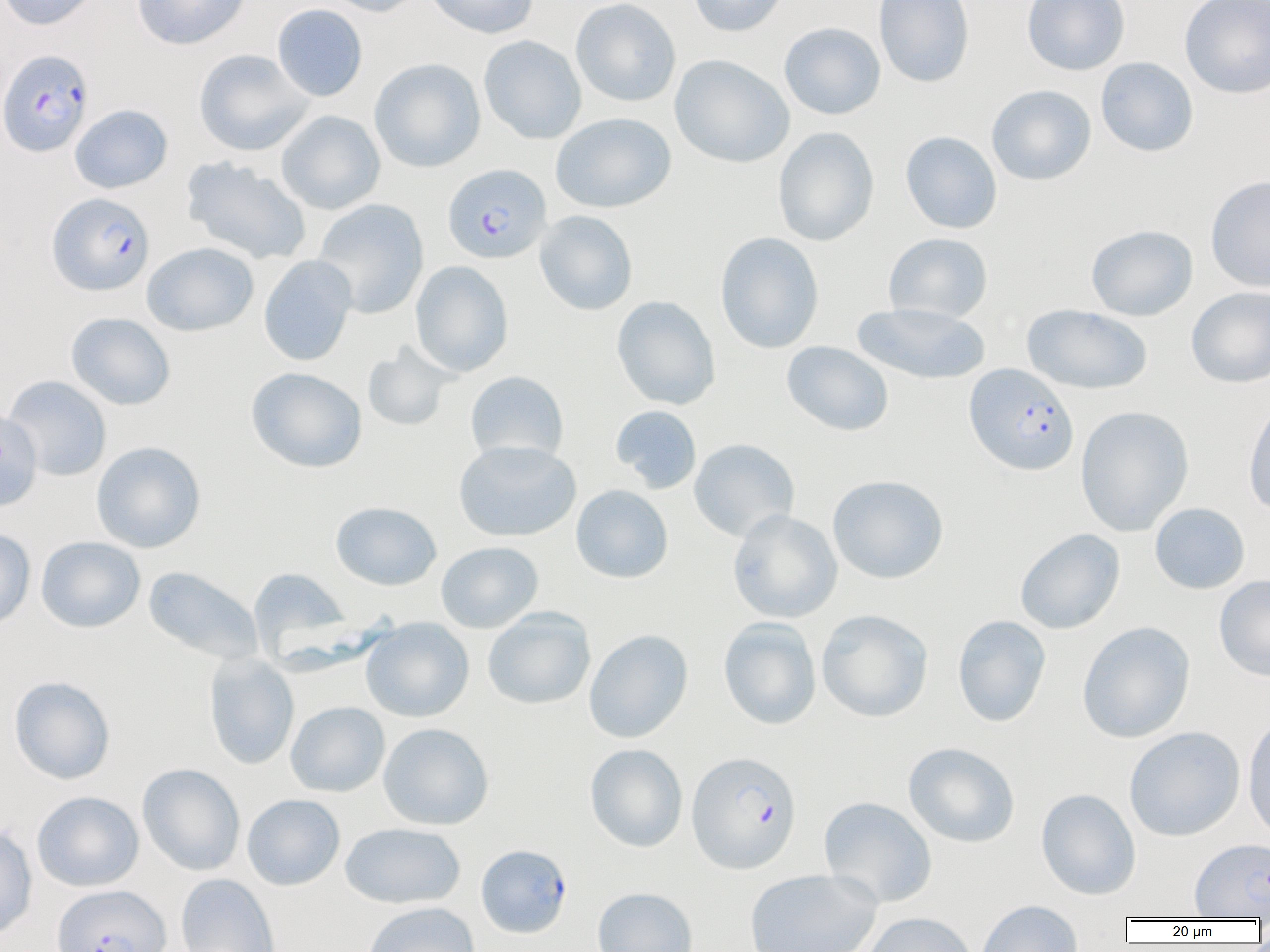
Approximate bounding boxes as named x1/y1/x2/y2 corners in pixels. Uninfected red blood cell locations: (x1=0, y1=0, x2=101, y2=30), (x1=132, y1=0, x2=251, y2=50), (x1=323, y1=0, x2=428, y2=17), (x1=424, y1=0, x2=539, y2=39), (x1=570, y1=0, x2=681, y2=107), (x1=686, y1=0, x2=789, y2=37), (x1=873, y1=0, x2=974, y2=87), (x1=1022, y1=0, x2=1130, y2=76), (x1=1179, y1=0, x2=1270, y2=98), (x1=272, y1=3, x2=368, y2=102), (x1=779, y1=22, x2=886, y2=120), (x1=478, y1=35, x2=586, y2=144), (x1=193, y1=49, x2=314, y2=156), (x1=669, y1=54, x2=795, y2=168), (x1=1096, y1=57, x2=1198, y2=157), (x1=369, y1=58, x2=486, y2=173), (x1=986, y1=84, x2=1097, y2=186), (x1=69, y1=104, x2=173, y2=194), (x1=276, y1=110, x2=385, y2=214), (x1=551, y1=112, x2=676, y2=214), (x1=772, y1=127, x2=879, y2=246), (x1=900, y1=131, x2=1002, y2=234), (x1=180, y1=156, x2=312, y2=265), (x1=1206, y1=176, x2=1270, y2=292), (x1=312, y1=198, x2=429, y2=319), (x1=535, y1=210, x2=638, y2=315), (x1=1085, y1=224, x2=1198, y2=321), (x1=715, y1=232, x2=824, y2=353), (x1=883, y1=232, x2=993, y2=324), (x1=141, y1=242, x2=259, y2=337), (x1=258, y1=255, x2=358, y2=367), (x1=410, y1=260, x2=514, y2=377), (x1=1186, y1=286, x2=1270, y2=388), (x1=611, y1=296, x2=721, y2=410), (x1=852, y1=302, x2=991, y2=386), (x1=1022, y1=304, x2=1153, y2=394), (x1=66, y1=312, x2=176, y2=410), (x1=781, y1=340, x2=894, y2=437), (x1=362, y1=344, x2=455, y2=432), (x1=245, y1=367, x2=367, y2=473), (x1=465, y1=371, x2=570, y2=465), (x1=3, y1=375, x2=112, y2=481), (x1=1243, y1=396, x2=1270, y2=516), (x1=610, y1=405, x2=702, y2=494), (x1=1075, y1=405, x2=1194, y2=536), (x1=0, y1=408, x2=42, y2=512), (x1=688, y1=438, x2=800, y2=542), (x1=454, y1=440, x2=581, y2=542), (x1=92, y1=441, x2=206, y2=553), (x1=827, y1=475, x2=948, y2=584), (x1=571, y1=485, x2=673, y2=583), (x1=330, y1=501, x2=442, y2=590), (x1=1149, y1=502, x2=1250, y2=594), (x1=727, y1=509, x2=842, y2=623), (x1=0, y1=528, x2=36, y2=631), (x1=1015, y1=528, x2=1125, y2=634), (x1=35, y1=536, x2=146, y2=633), (x1=435, y1=541, x2=544, y2=633), (x1=143, y1=566, x2=264, y2=666), (x1=248, y1=567, x2=352, y2=661), (x1=1214, y1=574, x2=1270, y2=682), (x1=482, y1=607, x2=596, y2=710), (x1=816, y1=609, x2=933, y2=722), (x1=952, y1=615, x2=1052, y2=727), (x1=718, y1=617, x2=821, y2=730), (x1=361, y1=618, x2=474, y2=722), (x1=1077, y1=621, x2=1195, y2=743), (x1=584, y1=629, x2=693, y2=743), (x1=203, y1=653, x2=300, y2=770), (x1=9, y1=675, x2=116, y2=784), (x1=285, y1=701, x2=390, y2=797), (x1=1242, y1=713, x2=1270, y2=844), (x1=378, y1=722, x2=494, y2=830), (x1=1123, y1=726, x2=1245, y2=842), (x1=903, y1=742, x2=1020, y2=848), (x1=585, y1=743, x2=688, y2=852), (x1=137, y1=763, x2=245, y2=876), (x1=1035, y1=788, x2=1141, y2=900), (x1=31, y1=791, x2=144, y2=891), (x1=242, y1=793, x2=345, y2=890), (x1=818, y1=796, x2=938, y2=908), (x1=340, y1=822, x2=466, y2=909), (x1=0, y1=824, x2=38, y2=941), (x1=1190, y1=838, x2=1270, y2=919), (x1=743, y1=868, x2=882, y2=952), (x1=175, y1=873, x2=280, y2=952), (x1=592, y1=887, x2=698, y2=952), (x1=975, y1=899, x2=1083, y2=952), (x1=362, y1=902, x2=480, y2=952), (x1=860, y1=912, x2=979, y2=952). Plasmodium falciparum-infected red blood cell locations: (x1=0, y1=49, x2=95, y2=157), (x1=443, y1=163, x2=551, y2=264), (x1=47, y1=192, x2=155, y2=295), (x1=964, y1=363, x2=1079, y2=475), (x1=686, y1=750, x2=802, y2=874), (x1=475, y1=844, x2=572, y2=938), (x1=51, y1=884, x2=171, y2=952). Slide-level diagnosis: Plasmodium falciparum. Single field of view. Thin blood smear. Image is 1270×952 pixels. Captured at 1000x magnification. Light microscopy.